Assess this cell for malaria.
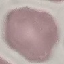
Uninfected.

preparation = thin blood film
capture = smartphone through the microscope eyepiece
stain = Giemsa
image type = cell patch, automatically extracted from a larger field of view and resized to 64 × 64 pixels